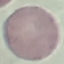

Malaria status: uninfected. Thin smear of blood. Cell patch, automatically extracted from a larger field of view and resized to 64 × 64 pixels. Giemsa-stained preparation. Photographed with a smartphone camera at the microscope eyepiece.